Identify the blood parasite species.
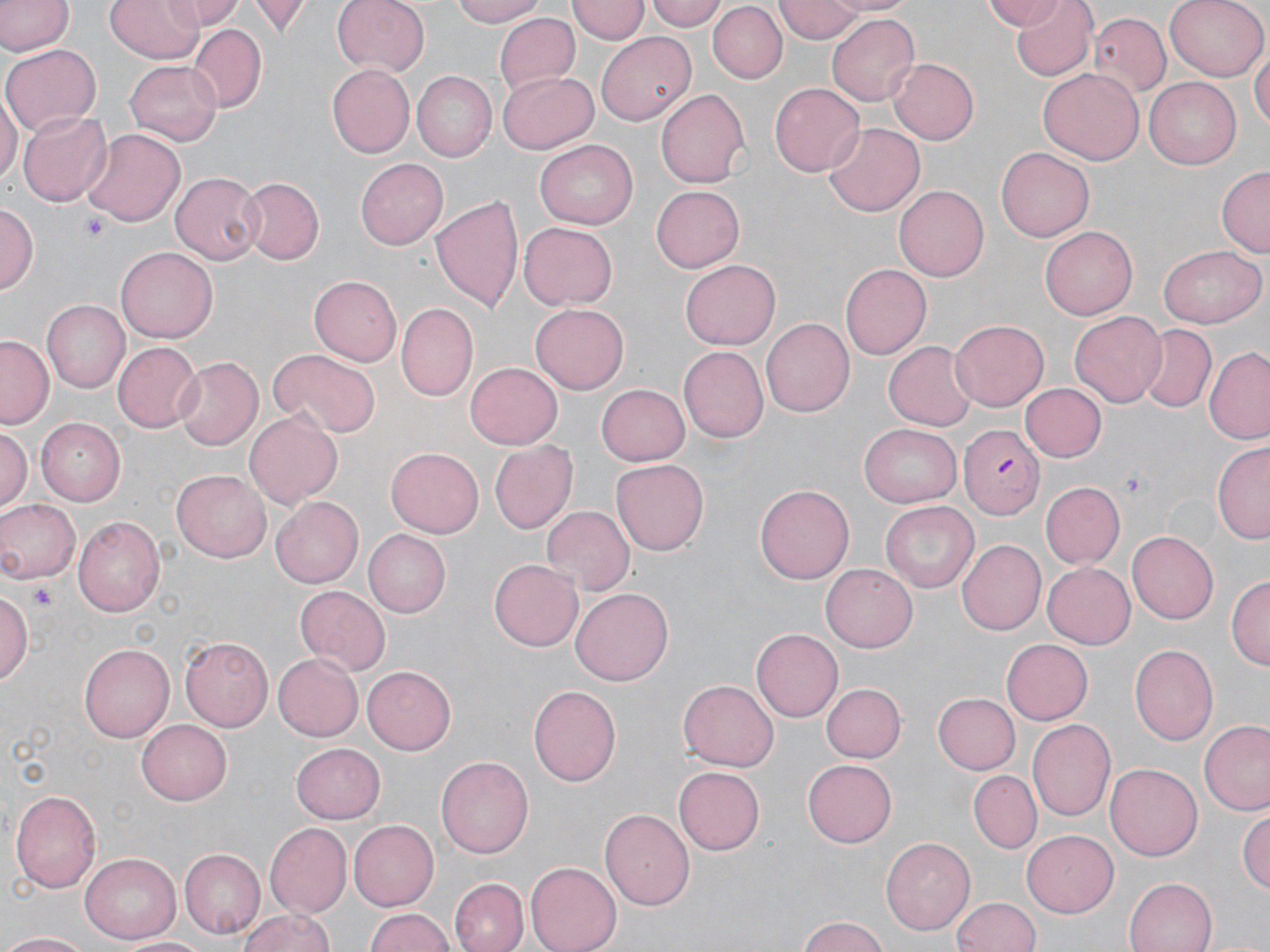

Plasmodium falciparum.

magnification = 1000x
image size = 1270×952 pixels
uninfected red blood cell locations = approximate bounding boxes as named x1/y1/x2/y2 corners in pixels: (x1=0, y1=0, x2=70, y2=56), (x1=105, y1=0, x2=203, y2=62), (x1=165, y1=0, x2=239, y2=31), (x1=250, y1=0, x2=308, y2=36), (x1=330, y1=0, x2=428, y2=74), (x1=450, y1=0, x2=553, y2=26), (x1=647, y1=0, x2=731, y2=31), (x1=820, y1=0, x2=917, y2=17), (x1=981, y1=0, x2=1070, y2=31), (x1=1008, y1=0, x2=1097, y2=81), (x1=1165, y1=0, x2=1269, y2=81), (x1=569, y1=1, x2=648, y2=45), (x1=774, y1=1, x2=864, y2=42), (x1=709, y1=4, x2=786, y2=82), (x1=495, y1=12, x2=580, y2=95), (x1=828, y1=13, x2=922, y2=107), (x1=1090, y1=13, x2=1173, y2=99), (x1=188, y1=25, x2=267, y2=111), (x1=597, y1=33, x2=698, y2=126), (x1=1251, y1=42, x2=1269, y2=138), (x1=3, y1=43, x2=99, y2=136), (x1=890, y1=57, x2=978, y2=144), (x1=126, y1=59, x2=222, y2=145), (x1=327, y1=65, x2=414, y2=156), (x1=1038, y1=68, x2=1143, y2=164), (x1=497, y1=72, x2=599, y2=154), (x1=410, y1=73, x2=495, y2=162), (x1=1146, y1=77, x2=1240, y2=168), (x1=769, y1=82, x2=865, y2=176), (x1=656, y1=87, x2=751, y2=190), (x1=0, y1=89, x2=19, y2=190), (x1=17, y1=110, x2=112, y2=205), (x1=822, y1=122, x2=927, y2=217), (x1=82, y1=127, x2=185, y2=225), (x1=535, y1=139, x2=640, y2=229), (x1=995, y1=145, x2=1094, y2=242), (x1=356, y1=157, x2=449, y2=249), (x1=1216, y1=165, x2=1270, y2=258), (x1=169, y1=171, x2=263, y2=265), (x1=237, y1=176, x2=323, y2=265), (x1=649, y1=184, x2=743, y2=274), (x1=895, y1=184, x2=989, y2=282), (x1=432, y1=196, x2=524, y2=314), (x1=0, y1=203, x2=37, y2=296), (x1=517, y1=223, x2=617, y2=310), (x1=1040, y1=226, x2=1137, y2=319), (x1=1158, y1=245, x2=1266, y2=329), (x1=115, y1=247, x2=216, y2=343), (x1=679, y1=260, x2=781, y2=349), (x1=839, y1=264, x2=931, y2=360), (x1=310, y1=275, x2=403, y2=365), (x1=41, y1=298, x2=130, y2=391), (x1=531, y1=303, x2=630, y2=393), (x1=396, y1=304, x2=478, y2=401), (x1=1070, y1=311, x2=1167, y2=408), (x1=761, y1=317, x2=853, y2=417), (x1=949, y1=319, x2=1050, y2=410), (x1=1138, y1=326, x2=1215, y2=412), (x1=0, y1=335, x2=54, y2=429), (x1=884, y1=340, x2=977, y2=431), (x1=112, y1=341, x2=201, y2=433), (x1=678, y1=345, x2=767, y2=443), (x1=1204, y1=347, x2=1270, y2=445), (x1=269, y1=350, x2=378, y2=440), (x1=173, y1=357, x2=263, y2=452), (x1=465, y1=361, x2=562, y2=449), (x1=595, y1=384, x2=689, y2=465), (x1=1020, y1=384, x2=1107, y2=462), (x1=245, y1=409, x2=342, y2=507), (x1=37, y1=418, x2=127, y2=506), (x1=861, y1=423, x2=962, y2=505), (x1=1, y1=424, x2=31, y2=509), (x1=488, y1=440, x2=578, y2=535), (x1=1212, y1=442, x2=1270, y2=544), (x1=386, y1=445, x2=483, y2=535), (x1=612, y1=457, x2=707, y2=550), (x1=173, y1=468, x2=274, y2=561), (x1=1042, y1=482, x2=1125, y2=567), (x1=755, y1=484, x2=851, y2=585), (x1=271, y1=496, x2=366, y2=589), (x1=0, y1=498, x2=81, y2=583), (x1=880, y1=501, x2=978, y2=593), (x1=542, y1=506, x2=634, y2=594), (x1=74, y1=517, x2=165, y2=617), (x1=363, y1=529, x2=450, y2=617), (x1=1128, y1=530, x2=1221, y2=623), (x1=957, y1=539, x2=1045, y2=635), (x1=489, y1=558, x2=583, y2=651), (x1=1044, y1=562, x2=1135, y2=649), (x1=821, y1=563, x2=917, y2=651), (x1=1227, y1=574, x2=1269, y2=670), (x1=295, y1=586, x2=390, y2=671), (x1=571, y1=588, x2=674, y2=685), (x1=0, y1=591, x2=33, y2=689), (x1=752, y1=628, x2=843, y2=722), (x1=179, y1=635, x2=273, y2=731), (x1=1002, y1=639, x2=1093, y2=723), (x1=80, y1=643, x2=178, y2=742), (x1=1129, y1=644, x2=1217, y2=744), (x1=273, y1=652, x2=363, y2=741), (x1=361, y1=666, x2=457, y2=754), (x1=676, y1=680, x2=778, y2=772), (x1=820, y1=682, x2=905, y2=762), (x1=528, y1=685, x2=623, y2=786), (x1=932, y1=692, x2=1020, y2=775), (x1=136, y1=718, x2=232, y2=804), (x1=1027, y1=718, x2=1117, y2=824), (x1=1200, y1=721, x2=1270, y2=816), (x1=293, y1=740, x2=386, y2=821), (x1=436, y1=755, x2=533, y2=859), (x1=801, y1=759, x2=896, y2=847), (x1=1105, y1=761, x2=1201, y2=859), (x1=675, y1=766, x2=765, y2=855), (x1=968, y1=771, x2=1043, y2=854), (x1=10, y1=788, x2=102, y2=893), (x1=1240, y1=807, x2=1270, y2=897), (x1=600, y1=809, x2=695, y2=910), (x1=345, y1=818, x2=439, y2=911), (x1=265, y1=822, x2=352, y2=918), (x1=1023, y1=828, x2=1119, y2=914), (x1=881, y1=838, x2=974, y2=935), (x1=179, y1=848, x2=264, y2=937), (x1=81, y1=854, x2=181, y2=943), (x1=526, y1=863, x2=620, y2=952), (x1=450, y1=876, x2=527, y2=952), (x1=1126, y1=876, x2=1217, y2=952), (x1=949, y1=897, x2=1044, y2=951), (x1=235, y1=907, x2=338, y2=952), (x1=364, y1=907, x2=455, y2=952), (x1=796, y1=916, x2=890, y2=951), (x1=1, y1=931, x2=93, y2=951), (x1=123, y1=935, x2=211, y2=952)
platelet locations = approximate bounding boxes as named x1/y1/x2/y2 corners in pixels: (x1=81, y1=213, x2=110, y2=241), (x1=1118, y1=469, x2=1149, y2=495), (x1=27, y1=579, x2=57, y2=609)
preparation = thin blood smear
stain = May-Grünwald-Giemsa
Plasmodium falciparum-infected red blood cell locations = approximate bounding boxes as named x1/y1/x2/y2 corners in pixels: (x1=961, y1=426, x2=1045, y2=517)
field of view = one of a larger specimen
modality = light microscopy